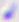
modality = micrograph
identification = Toxoplasma gondii
magnification = 400x